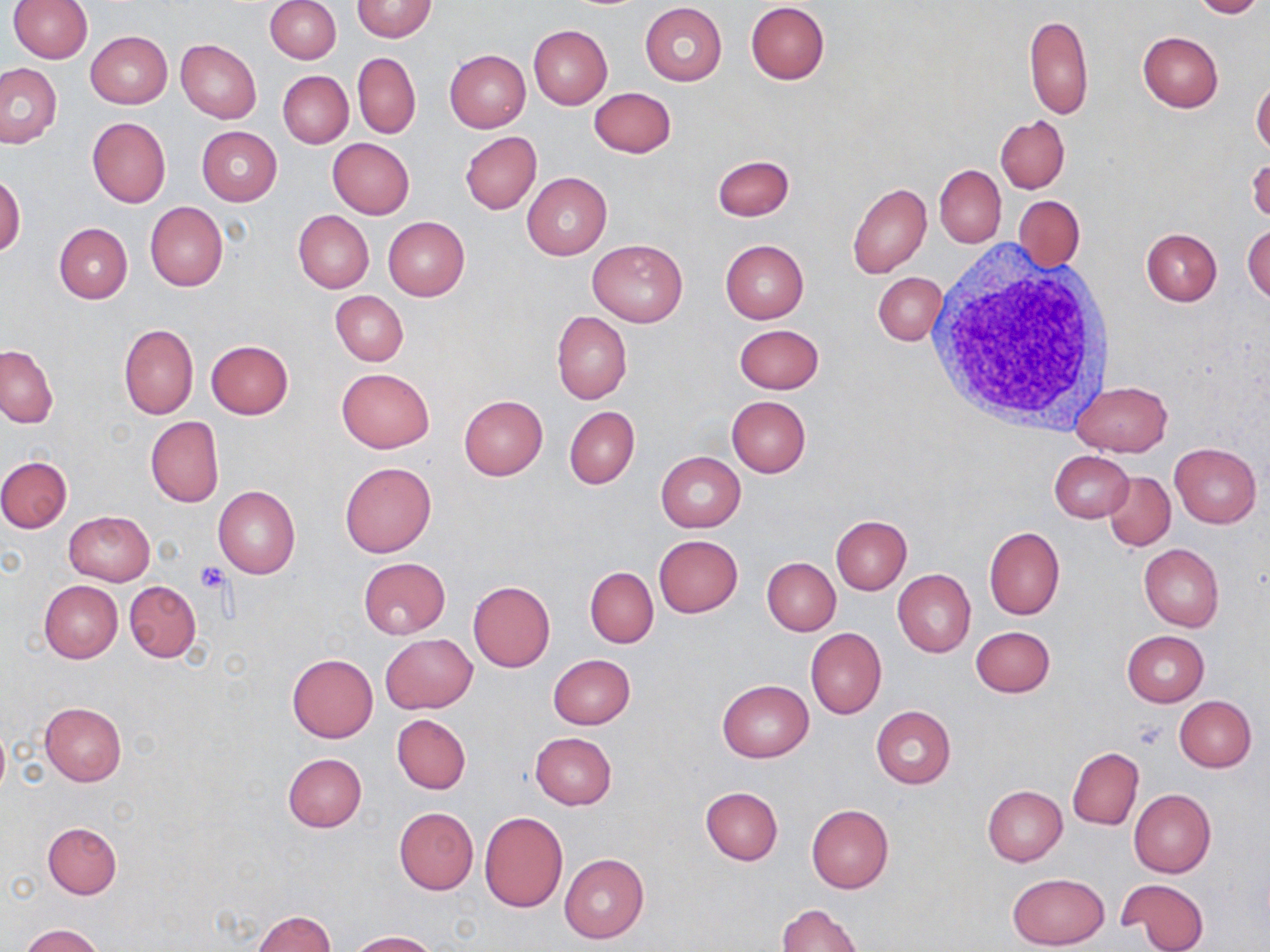

slide-level diagnosis = no evidence of blood parasites
white blood cell locations = approximate bounding boxes as [x1, y1, x2, y2] in pixels: [928, 248, 1118, 433]
preparation = thin blood film
uninfected red blood cell locations = approximate bounding boxes as [x1, y1, x2, y2] in pixels: [8, 0, 92, 63], [266, 0, 341, 63], [351, 0, 438, 43], [1192, 0, 1264, 18], [745, 2, 829, 83], [640, 3, 728, 85], [1023, 15, 1093, 119], [529, 25, 612, 109], [86, 30, 171, 108], [1137, 31, 1223, 112], [176, 40, 261, 124], [444, 50, 530, 132], [353, 52, 421, 139], [0, 63, 62, 149], [278, 71, 353, 148], [1251, 77, 1270, 152], [589, 87, 676, 158], [996, 115, 1070, 192], [87, 116, 170, 209], [196, 126, 282, 205], [461, 131, 541, 215], [327, 137, 413, 219], [712, 155, 794, 220], [1247, 157, 1270, 222], [934, 164, 1006, 248], [521, 173, 612, 260], [0, 174, 25, 257], [847, 181, 931, 279], [1014, 195, 1083, 273], [145, 202, 228, 291], [293, 210, 374, 292], [383, 216, 469, 301], [1243, 221, 1270, 304], [54, 223, 132, 304], [1141, 227, 1222, 306], [588, 238, 688, 326], [721, 240, 809, 323], [873, 272, 946, 346], [331, 291, 408, 366], [551, 310, 632, 404], [119, 323, 198, 419], [733, 324, 824, 394], [206, 340, 293, 418], [0, 344, 57, 427], [337, 368, 435, 452], [1070, 380, 1172, 455], [459, 396, 548, 480], [726, 396, 810, 477], [564, 406, 639, 489], [146, 417, 223, 507], [1169, 442, 1262, 528], [1049, 451, 1134, 523], [656, 452, 745, 532], [0, 456, 72, 532], [340, 462, 436, 558], [1104, 471, 1175, 550], [214, 486, 300, 578], [63, 511, 154, 586], [831, 515, 912, 595], [984, 526, 1065, 620], [654, 535, 743, 617], [1139, 544, 1223, 632], [358, 557, 451, 639], [762, 558, 840, 635], [585, 567, 658, 647], [892, 569, 975, 657], [39, 580, 123, 662], [125, 581, 200, 661], [468, 581, 555, 672], [971, 626, 1054, 698], [805, 627, 886, 719], [1120, 630, 1208, 707], [380, 633, 477, 713], [287, 654, 378, 742], [543, 654, 628, 807], [548, 654, 635, 730], [718, 680, 812, 762], [1175, 696, 1256, 772], [40, 701, 126, 785], [871, 706, 956, 789], [393, 714, 470, 793], [530, 732, 617, 810], [1067, 749, 1144, 830], [282, 753, 366, 832], [982, 785, 1067, 866], [701, 786, 783, 865], [1129, 789, 1215, 878], [806, 804, 893, 893], [393, 807, 478, 895], [479, 811, 570, 912], [44, 821, 121, 898], [560, 854, 649, 943], [1006, 872, 1110, 950], [1118, 878, 1210, 950], [776, 904, 863, 951], [252, 910, 334, 952], [20, 923, 105, 952], [347, 930, 434, 951]
field of view = one of a larger specimen
stain = May-Grünwald-Giemsa
image size = 1270×952 pixels
platelet locations = approximate bounding boxes as [x1, y1, x2, y2] in pixels: [194, 561, 228, 592]
modality = light microscopy
magnification = 1000x